Evaluate for Plasmodium parasites.
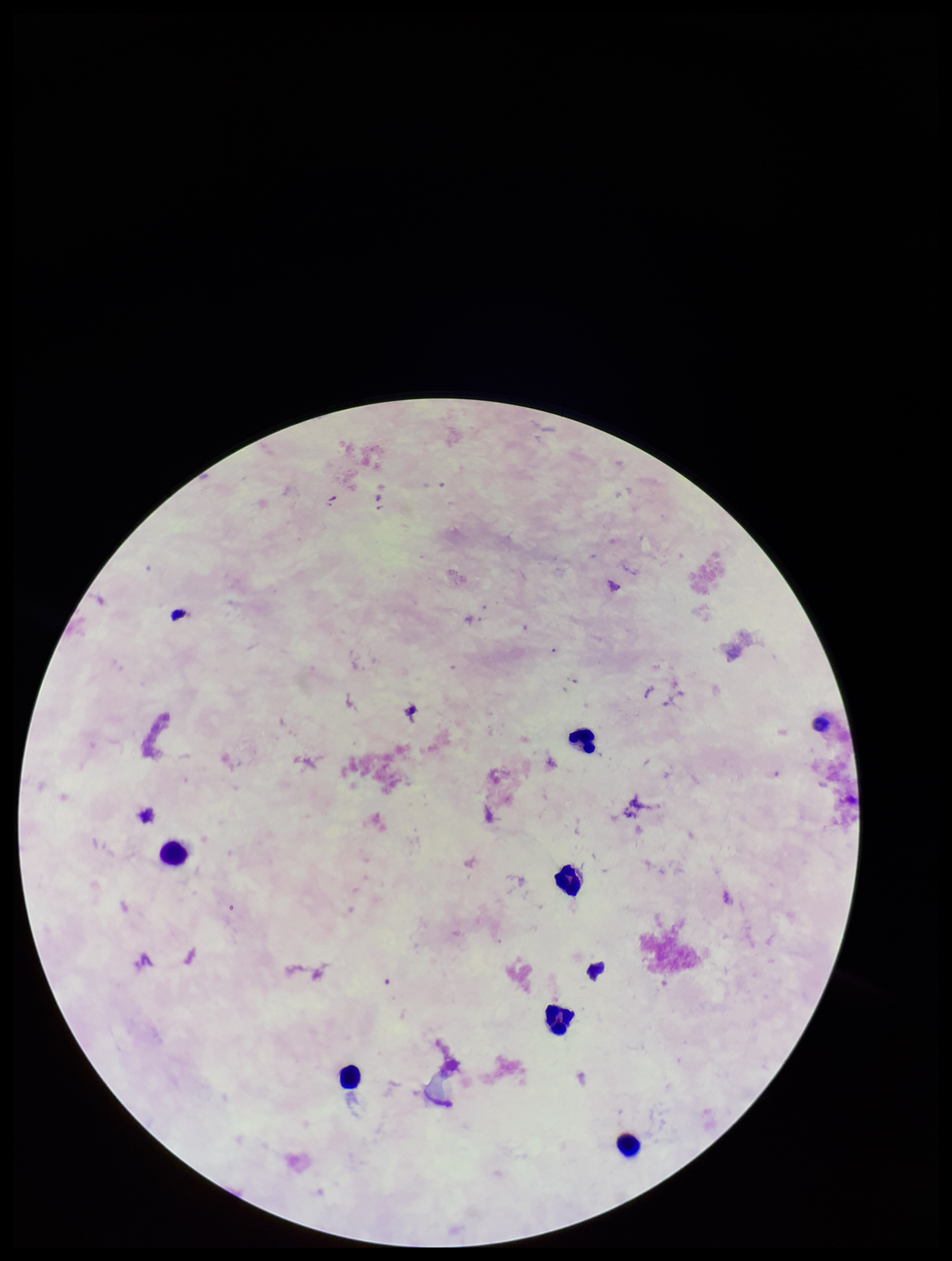

None detected.

Single field of view. Image is 952×1261 pixels. Preparation: thick blood smear. Parasite count: 0. Patient malaria status: negative. Smartphone photograph taken through the eyepiece of a microscope. Giemsa stain. Leukocyte count: 6.